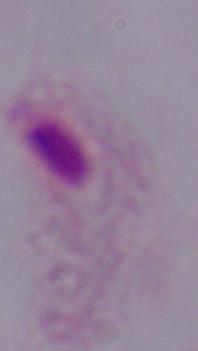

Summary:
  - Identification: trichomonad
  - Modality: micrograph
  - Magnification: 1000x